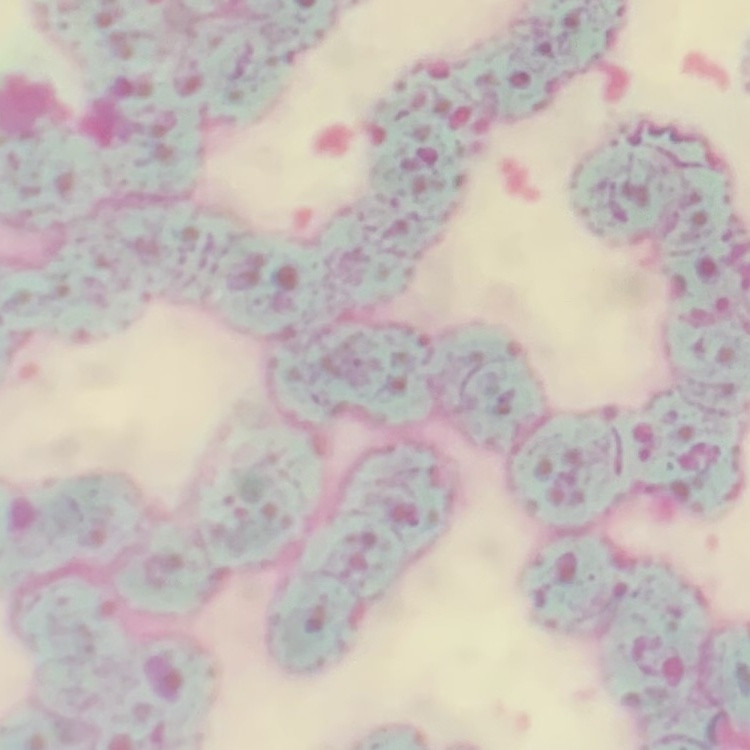

The erythrocytes show rouleaux formation. Thin peripheral smear. Square crop of a larger photomicrograph. Field's or Giemsa stain.